State which parasite is depicted.
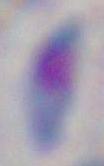

Toxoplasma gondii.

magnification = 1000x
modality = photomicrograph